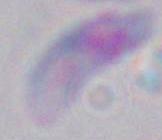
Photomicrograph. 1000x magnification. Toxoplasma gondii is shown.